State the blood parasite species.
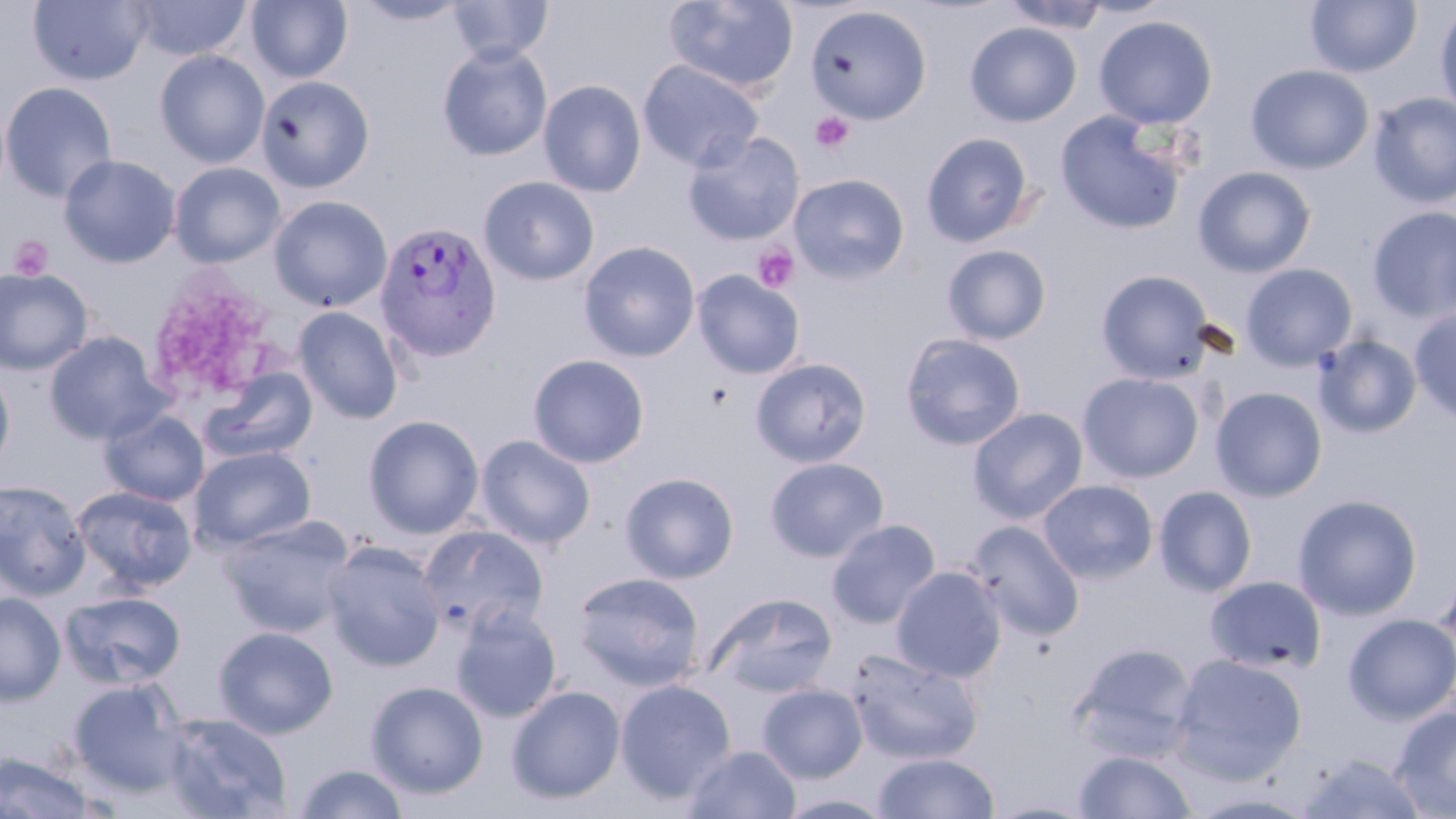

Plasmodium vivax.

preparation: thin blood smear
modality: optical microscopy
magnification: 1000x
plasmodium_vivax_infected_red_blood_cell_locations: 'approximate bounding boxes as (x1,y1)-(x2,y2) corner pairs in pixels: (375,220)-(503,362)'
platelet_locations: 'approximate bounding boxes as (x1,y1)-(x2,y2) corner pairs in pixels: (810,111)-(854,154), (7,235)-(53,280), (753,243)-(799,293)'
image_size: 1456×819 pixels
stain: May-Grünwald-Giemsa
field_of_view: single
uninfected_red_blood_cell_locations: 'approximate bounding boxes as (x1,y1)-(x2,y2) corner pairs in pixels: (28,0)-(152,86), (353,0)-(471,25), (447,0)-(553,64), (664,0)-(800,94), (1076,0)-(1176,19), (129,1)-(253,61), (245,1)-(353,84), (1002,1)-(1112,34), (1305,1)-(1422,76), (1434,2)-(1456,123), (805,5)-(932,124), (1093,15)-(1218,130), (964,22)-(1082,126), (437,44)-(553,161), (154,50)-(270,168), (638,61)-(764,173), (1245,64)-(1375,174), (256,75)-(375,193), (538,80)-(646,197), (1,81)-(118,203), (1367,92)-(1456,208), (1055,112)-(1187,235), (683,131)-(804,246), (921,132)-(1034,248), (58,154)-(181,268), (169,162)-(286,268), (1192,166)-(1316,278), (789,174)-(910,284), (479,176)-(599,286), (268,195)-(392,312), (1366,205)-(1456,323), (578,241)-(700,362), (942,244)-(1052,345), (1240,263)-(1357,370), (0,267)-(93,375), (692,270)-(805,380), (1096,270)-(1214,383), (294,307)-(403,425), (1409,307)-(1456,423), (43,332)-(169,446), (900,333)-(1027,450), (1313,334)-(1423,438), (527,354)-(650,467), (750,357)-(872,468), (0,362)-(15,478), (201,366)-(319,464), (1078,372)-(1204,483), (1079,382)-(1329,489), (1210,387)-(1327,502), (99,408)-(209,505), (968,408)-(1088,525), (363,415)-(485,539), (475,434)-(596,550), (189,446)-(316,551), (764,457)-(888,562), (619,472)-(740,583), (0,479)-(91,600), (1038,480)-(1158,583), (71,485)-(198,593), (1153,486)-(1257,597), (1292,494)-(1423,620), (219,514)-(357,638), (826,518)-(941,628), (967,520)-(1085,642), (419,524)-(550,638), (321,540)-(447,672), (1435,563)-(1456,674), (891,566)-(1006,683), (573,571)-(705,690), (1205,575)-(1327,674), (60,591)-(186,688), (0,592)-(66,706), (708,592)-(837,698), (450,604)-(562,723), (1343,614)-(1456,724), (213,625)-(338,739), (1070,642)-(1198,761), (846,648)-(983,765), (1170,653)-(1307,783), (68,678)-(188,796), (614,679)-(737,804), (365,681)-(489,798), (758,684)-(867,782), (506,685)-(626,804), (1391,707)-(1456,818), (160,712)-(293,818), (684,744)-(801,819), (1073,750)-(1196,818), (0,751)-(95,819), (872,752)-(999,818), (1296,752)-(1427,819), (295,763)-(409,819), (775,792)-(896,818), (985,798)-(1100,818)'